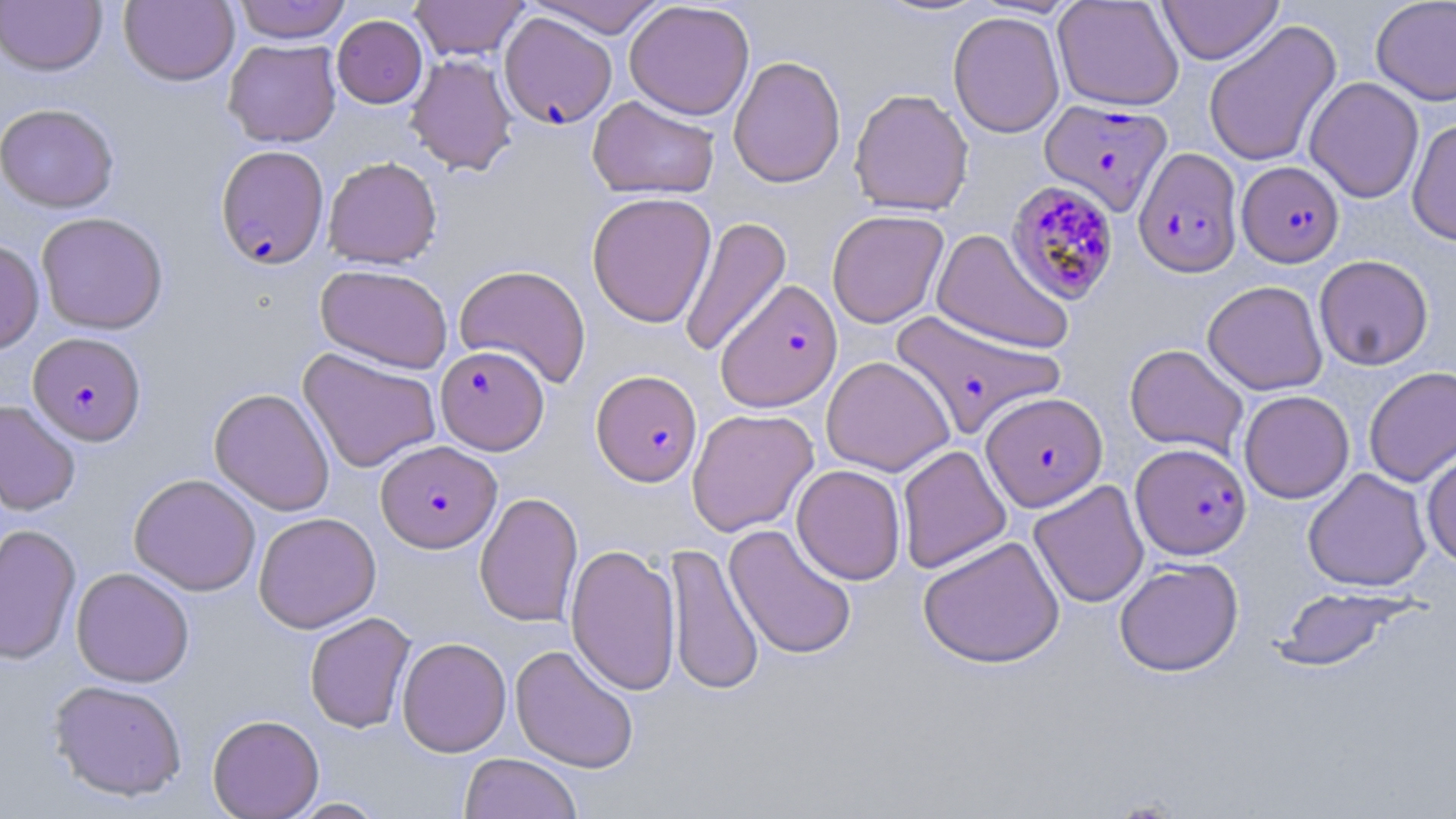
Plasmodium falciparum-infected red blood cell locations = approximate bounding boxes as named x1/y1/x2/y2 corners in pixels: (x1=499, y1=12, x2=617, y2=129), (x1=1039, y1=98, x2=1171, y2=215), (x1=215, y1=145, x2=329, y2=268), (x1=1133, y1=147, x2=1243, y2=278), (x1=1237, y1=161, x2=1344, y2=267), (x1=1006, y1=180, x2=1120, y2=305), (x1=715, y1=279, x2=843, y2=412), (x1=890, y1=309, x2=1064, y2=439), (x1=28, y1=331, x2=146, y2=446), (x1=435, y1=345, x2=549, y2=454), (x1=591, y1=370, x2=702, y2=486), (x1=981, y1=392, x2=1107, y2=511), (x1=376, y1=440, x2=500, y2=552), (x1=1131, y1=442, x2=1251, y2=559)
slide-level diagnosis = Plasmodium falciparum
preparation = thin blood film
image size = 1456×819 pixels
magnification = 1000x
uninfected red blood cell locations = approximate bounding boxes as named x1/y1/x2/y2 corners in pixels: (x1=119, y1=0, x2=239, y2=86), (x1=233, y1=0, x2=352, y2=43), (x1=409, y1=0, x2=529, y2=61), (x1=526, y1=0, x2=669, y2=38), (x1=869, y1=0, x2=995, y2=18), (x1=1052, y1=0, x2=1184, y2=111), (x1=1157, y1=0, x2=1283, y2=64), (x1=1371, y1=0, x2=1456, y2=106), (x1=1, y1=1, x2=107, y2=75), (x1=624, y1=1, x2=754, y2=120), (x1=948, y1=11, x2=1065, y2=138), (x1=332, y1=14, x2=427, y2=108), (x1=1203, y1=20, x2=1342, y2=168), (x1=224, y1=39, x2=341, y2=147), (x1=405, y1=53, x2=518, y2=175), (x1=728, y1=55, x2=846, y2=188), (x1=1304, y1=77, x2=1424, y2=203), (x1=849, y1=88, x2=974, y2=216), (x1=587, y1=95, x2=719, y2=200), (x1=0, y1=103, x2=119, y2=212), (x1=1407, y1=118, x2=1456, y2=247), (x1=323, y1=156, x2=442, y2=269), (x1=586, y1=192, x2=717, y2=328), (x1=826, y1=209, x2=949, y2=328), (x1=36, y1=212, x2=169, y2=334), (x1=678, y1=215, x2=792, y2=359), (x1=931, y1=228, x2=1074, y2=355), (x1=0, y1=240, x2=44, y2=354), (x1=1314, y1=255, x2=1433, y2=370), (x1=315, y1=263, x2=452, y2=374), (x1=453, y1=264, x2=592, y2=388), (x1=1202, y1=280, x2=1327, y2=395), (x1=1125, y1=343, x2=1249, y2=458), (x1=298, y1=348, x2=442, y2=473), (x1=821, y1=356, x2=955, y2=476), (x1=1364, y1=366, x2=1456, y2=487), (x1=209, y1=387, x2=335, y2=515), (x1=1239, y1=390, x2=1354, y2=504), (x1=0, y1=400, x2=81, y2=516), (x1=687, y1=408, x2=819, y2=537), (x1=897, y1=445, x2=1012, y2=574), (x1=1421, y1=448, x2=1456, y2=569), (x1=791, y1=464, x2=906, y2=585), (x1=1303, y1=468, x2=1431, y2=592), (x1=129, y1=473, x2=261, y2=596), (x1=1028, y1=480, x2=1149, y2=608), (x1=475, y1=491, x2=583, y2=628), (x1=253, y1=512, x2=381, y2=633), (x1=0, y1=523, x2=81, y2=665), (x1=724, y1=523, x2=857, y2=660), (x1=918, y1=535, x2=1065, y2=668), (x1=664, y1=542, x2=763, y2=697), (x1=565, y1=544, x2=681, y2=696), (x1=1114, y1=558, x2=1244, y2=676), (x1=71, y1=567, x2=195, y2=687), (x1=1273, y1=586, x2=1415, y2=672), (x1=304, y1=612, x2=416, y2=733), (x1=397, y1=637, x2=511, y2=757), (x1=510, y1=643, x2=639, y2=774), (x1=48, y1=679, x2=188, y2=801), (x1=207, y1=714, x2=324, y2=819), (x1=459, y1=753, x2=583, y2=819), (x1=285, y1=797, x2=388, y2=818)
modality = light microscopy
stain = May-Grünwald-Giemsa
field of view = one of a larger specimen